Name the cell type shown.
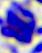

This is a leukocyte.

Summary:
  - Magnification: 400x
  - Modality: micrograph